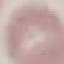

Malaria status: uninfected. Thin blood film. Giemsa-stained preparation. Automatically extracted cell patch, resized to 64 × 64 pixels. Photographed with a smartphone camera at the microscope eyepiece.